Assess this cell for malaria.
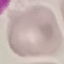

It is uninfected.

capture = smartphone camera at the microscope eyepiece
preparation = thin blood smear
stain = Giemsa
image type = automatically extracted cell patch, resized to 64 × 64 pixels